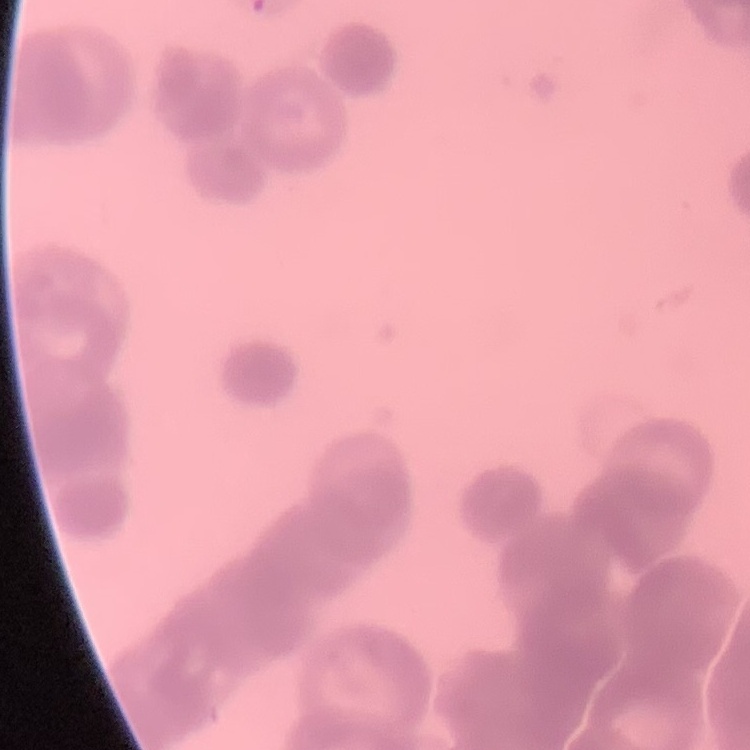

erythrocyte morphology = rouleaux formation
image type = square crop of a larger photomicrograph
preparation = thin blood smear
stain = Field's or Giemsa